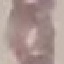
{
  "result": "no malaria parasites seen",
  "capture": "smartphone camera at the microscope eyepiece",
  "stain": "Giemsa",
  "preparation": "thin smear",
  "image_type": "automatically extracted cell patch, resized to 64 × 64 pixels"
}